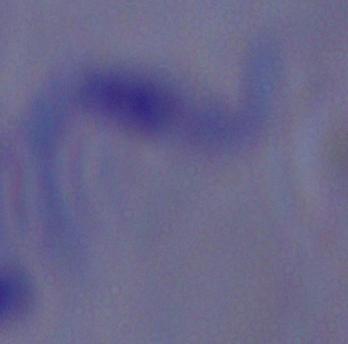

A trypanosome is seen. Photomicrograph. Captured at 1000x magnification.